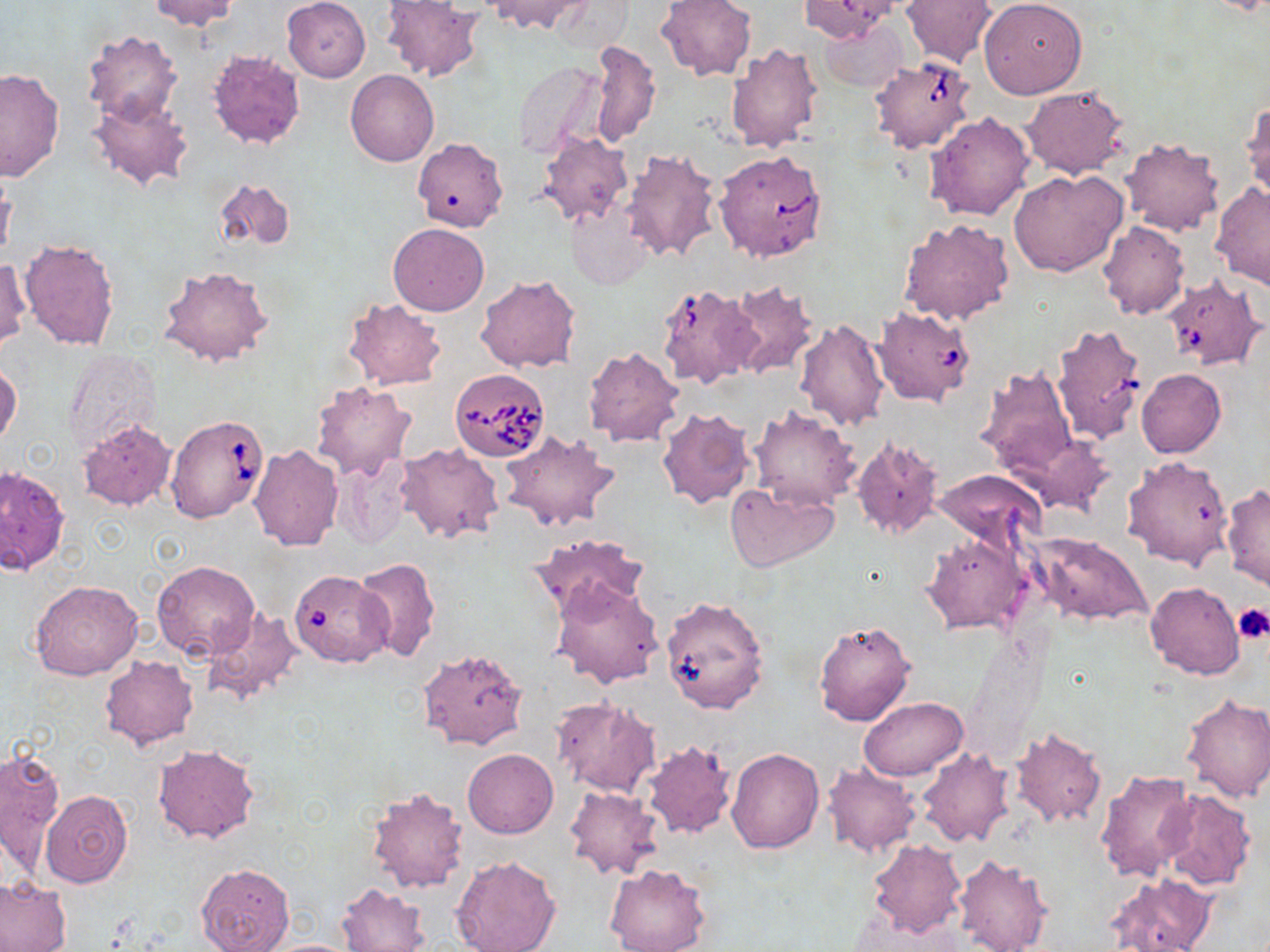 Approximate bounding boxes as [x1, y1, x2, y2] in pixels. Platelet locations: [1232, 603, 1270, 643]. Babesia divergens-infected red blood cell locations: [870, 56, 976, 155], [714, 150, 828, 262], [1161, 274, 1266, 371], [656, 283, 759, 390], [873, 305, 975, 407], [1051, 322, 1147, 443], [449, 368, 551, 461], [165, 414, 266, 523], [288, 570, 400, 669]. Uninfected red blood cell locations: [148, 0, 241, 32], [281, 0, 371, 82], [484, 0, 591, 35], [656, 0, 756, 82], [799, 0, 900, 41], [902, 0, 996, 68], [979, 0, 1087, 99], [378, 1, 484, 82], [819, 20, 904, 91], [81, 30, 183, 129], [589, 39, 659, 147], [722, 42, 824, 154], [207, 51, 306, 149], [512, 60, 605, 160], [0, 68, 65, 180], [346, 70, 439, 167], [1021, 84, 1129, 179], [87, 94, 194, 194], [1242, 99, 1269, 206], [925, 112, 1035, 222], [535, 131, 634, 226], [1118, 137, 1224, 236], [412, 138, 509, 233], [620, 147, 725, 263], [0, 164, 16, 266], [1009, 169, 1127, 278], [212, 178, 295, 253], [1210, 182, 1270, 290], [566, 204, 652, 290], [899, 217, 1014, 325], [1097, 221, 1190, 320], [388, 222, 489, 316], [19, 237, 121, 352], [0, 255, 31, 351], [157, 264, 273, 366], [476, 274, 582, 372], [723, 280, 817, 379], [342, 298, 447, 391], [795, 319, 890, 430], [583, 347, 684, 447], [62, 349, 159, 458], [0, 364, 21, 447], [973, 365, 1078, 477], [1137, 368, 1225, 458], [310, 381, 417, 481], [656, 406, 755, 508], [748, 406, 861, 512], [77, 419, 178, 512], [499, 430, 621, 531], [1024, 433, 1116, 516], [851, 435, 945, 542], [396, 443, 505, 545], [249, 444, 343, 551], [331, 454, 419, 549], [1122, 455, 1236, 571], [0, 465, 68, 575], [933, 470, 1047, 551], [724, 481, 840, 572], [1221, 484, 1269, 590], [921, 531, 1029, 635], [1026, 531, 1153, 628], [527, 532, 649, 618], [351, 556, 440, 661], [152, 560, 261, 662], [552, 579, 663, 689], [29, 581, 143, 680], [1145, 581, 1244, 680], [664, 590, 762, 716], [202, 609, 304, 708], [813, 619, 917, 727], [416, 648, 529, 751], [99, 655, 198, 749], [1180, 693, 1270, 802], [859, 696, 969, 780], [551, 697, 660, 798], [1008, 726, 1107, 828], [640, 741, 736, 839], [152, 744, 259, 843], [1, 746, 65, 876], [726, 747, 824, 853], [463, 748, 558, 838], [916, 748, 1015, 847], [821, 763, 922, 858], [1093, 768, 1197, 882], [364, 786, 469, 894], [563, 786, 662, 880], [39, 789, 133, 887], [1156, 789, 1257, 891], [867, 839, 966, 937], [952, 852, 1053, 952], [451, 855, 561, 952], [196, 861, 295, 952], [605, 863, 713, 952], [1106, 872, 1216, 952], [0, 879, 71, 952], [339, 883, 429, 952], [256, 938, 362, 952]. Slide-level diagnosis: Babesia divergens. Light microscopy. Captured at 1000x magnification. Image is 1270×952 pixels. Single field of view. Thin blood smear. May-Grünwald-Giemsa stain.